Give the location of every parasitized RBC.
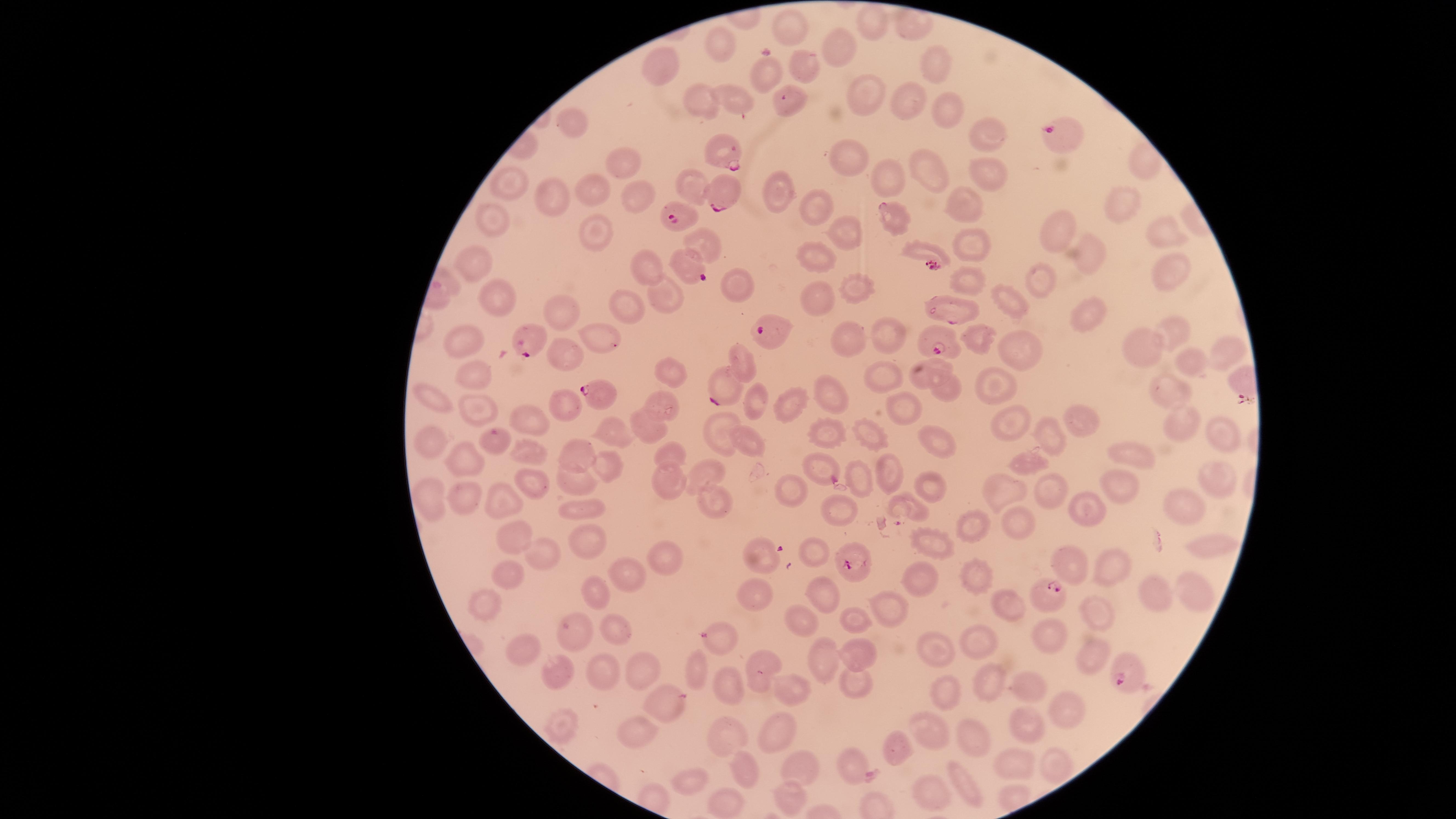

Approximate marker points as {x, y} in pixels.
Parasitized RBCs: {1054, 131}, {720, 152}, {721, 197}, {681, 218}, {935, 254}, {695, 273}, {763, 327}, {524, 338}, {939, 342}, {723, 389}, {595, 391}, {847, 562}, {1047, 596}, {1129, 677}.

visible region = circular
uninfected RBCs = approximate marker points as {x, y} in pixels: {873, 26}, {790, 33}, {713, 45}, {837, 49}, {939, 61}, {664, 65}, {803, 71}, {764, 74}, {871, 92}, {915, 99}, {696, 101}, {790, 107}, {739, 108}, {948, 110}, {570, 131}, {987, 138}, {1146, 159}, {622, 162}, {852, 162}, {983, 167}, {932, 170}, {897, 179}, {694, 183}, {517, 184}, {593, 189}, {555, 193}, {780, 195}, {641, 198}, {961, 201}, {1115, 209}, {811, 215}, {892, 217}, {493, 220}, {1050, 225}, {843, 231}, {1163, 234}, {703, 238}, {969, 238}, {605, 240}, {1088, 252}, {824, 256}, {476, 263}, {655, 269}, {1035, 269}, {1168, 270}, {965, 279}, {741, 287}, {663, 289}, {859, 292}, {819, 295}, {492, 299}, {629, 302}, {1011, 302}, {956, 307}, {568, 309}, {1084, 317}, {1168, 329}, {588, 333}, {855, 333}, {879, 336}, {982, 338}, {468, 347}, {1146, 351}, {1018, 353}, {566, 354}, {1225, 355}, {745, 357}, {1190, 370}, {661, 371}, {472, 377}, {924, 378}, {889, 381}, {996, 389}, {951, 390}, {1167, 395}, {830, 397}, {435, 398}, {559, 402}, {474, 405}, {667, 406}, {901, 406}, {756, 410}, {795, 411}, {1075, 412}, {530, 418}, {1184, 421}, {650, 426}, {718, 427}, {608, 428}, {1007, 429}, {828, 431}, {870, 433}, {1217, 436}, {1051, 438}, {430, 439}, {751, 441}, {937, 442}, {527, 447}, {1126, 448}, {671, 450}, {461, 451}, {578, 451}, {819, 463}, {1026, 463}, {603, 464}, {893, 469}, {706, 473}, {1216, 476}, {669, 480}, {574, 482}, {862, 483}, {528, 484}, {931, 485}, {1047, 487}, {1118, 488}, {1004, 492}, {792, 493}, {432, 496}, {465, 496}, {713, 496}, {504, 499}, {908, 505}, {1185, 508}, {584, 509}, {1082, 510}, {842, 513}, {1019, 524}, {515, 531}, {975, 531}, {581, 533}, {1202, 545}, {933, 547}, {542, 548}, {815, 550}, {757, 554}, {668, 556}, {1112, 565}, {1074, 566}, {512, 574}, {625, 577}, {978, 578}, {914, 582}, {1194, 584}, {755, 592}, {825, 592}, {1159, 595}, {596, 597}, {485, 604}, {1006, 605}, {1095, 605}, {888, 615}, {802, 619}, {857, 623}, {577, 630}, {614, 632}, {1052, 639}, {720, 640}, {979, 641}, {936, 649}, {523, 651}, {1094, 652}, {858, 654}, {821, 655}, {553, 665}, {640, 665}, {759, 666}, {697, 671}, {607, 679}, {725, 680}, {857, 681}, {793, 684}, {985, 685}, {1026, 685}, {945, 690}, {663, 696}, {1058, 710}, {1027, 723}, {558, 725}, {935, 731}, {778, 732}, {723, 733}, {638, 735}, {971, 739}, {898, 751}, {1051, 758}, {852, 764}, {802, 768}, {1009, 768}, {745, 776}, {690, 779}, {963, 780}, {789, 797}, {925, 798}, {720, 804}
preparation = thin smear of blood
species = Plasmodium falciparum
stain = Giemsa
capture = smartphone photograph through the microscope eyepiece
field of view = single
image size = 1456×819 pixels